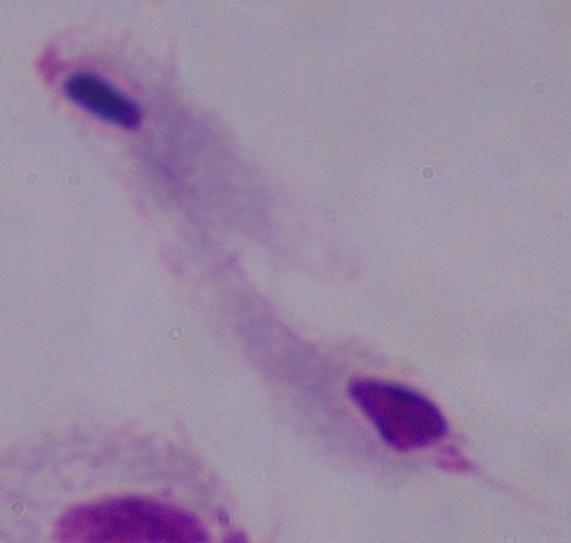

A trichomonad is shown. Micrograph. 1000x magnification.